Assess this cell for malaria.
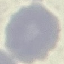
It is uninfected.

Cell patch, automatically extracted from a larger field of view and resized to 64 × 64 pixels. Giemsa stain. Acquired by smartphone through the microscope eyepiece. Thin smear of blood.